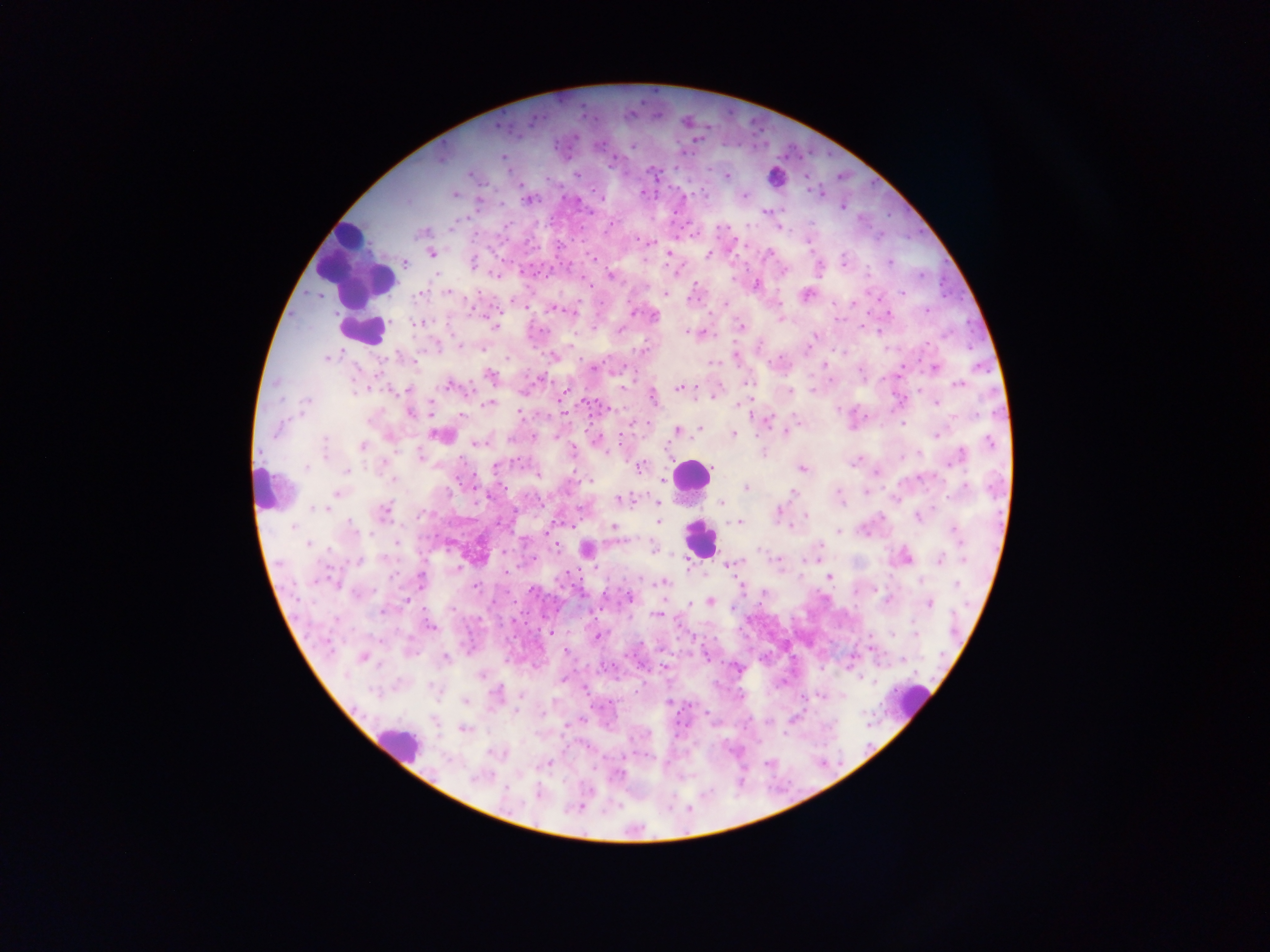 Approximate centers as [x, y] in pixels. Plasmodium parasite locations: [656, 91], [644, 100], [582, 105], [731, 110], [544, 114], [657, 115], [597, 118], [752, 120], [686, 122], [706, 124], [497, 125], [532, 126], [764, 131], [574, 137], [693, 141], [636, 144], [676, 144], [791, 144], [603, 150], [812, 152], [828, 153], [568, 155], [503, 156], [440, 158], [679, 165], [653, 173], [837, 175], [726, 176], [806, 178], [871, 181], [703, 186], [593, 190], [642, 192], [820, 192], [454, 194], [565, 194], [685, 195], [707, 195], [743, 196], [602, 197], [528, 199], [843, 206], [906, 209], [590, 211], [674, 212], [889, 213], [556, 215], [551, 224], [609, 226], [779, 226], [422, 232], [924, 233], [694, 234], [498, 235], [558, 237], [808, 238], [906, 238], [525, 240], [649, 243], [814, 250], [432, 253], [586, 253], [669, 253], [708, 254], [556, 256], [501, 258], [595, 259], [512, 260], [404, 262], [472, 262], [529, 262], [819, 262], [842, 262], [890, 262], [571, 263], [782, 270], [521, 273], [920, 273], [498, 274], [535, 274], [868, 274], [610, 275], [548, 278], [583, 278], [939, 281], [756, 284], [592, 285], [447, 291], [805, 293], [902, 293], [419, 294], [665, 294], [688, 299], [834, 301], [853, 301], [725, 305], [524, 306], [924, 308], [553, 309], [866, 310], [633, 312], [888, 314], [653, 315], [835, 317], [844, 317], [780, 319], [967, 319], [415, 322], [861, 325], [494, 326], [740, 327], [620, 330], [688, 331], [694, 332], [701, 332], [814, 336], [928, 340], [460, 346], [635, 346], [969, 346], [735, 355], [327, 357], [554, 357], [976, 362], [823, 365], [625, 366], [593, 368], [935, 368], [490, 376], [748, 383], [450, 384], [959, 384], [680, 388], [788, 391], [714, 394], [562, 397], [652, 397], [581, 399], [596, 399], [305, 402], [935, 402], [489, 404], [743, 404], [430, 408], [606, 408], [409, 410], [519, 410], [588, 416], [549, 419], [767, 419], [523, 421], [649, 422], [902, 424], [700, 429], [621, 430], [678, 431], [786, 432], [534, 434], [733, 434], [936, 434], [441, 435], [556, 435], [596, 439], [477, 442], [362, 447], [764, 454], [573, 455], [461, 458], [518, 459], [494, 465], [639, 467], [801, 468], [574, 470], [345, 472], [876, 472], [474, 475], [537, 477], [593, 477], [392, 480], [663, 481], [459, 484], [503, 487], [746, 488], [866, 492], [792, 493], [336, 494], [488, 495], [619, 499], [721, 503], [657, 504], [472, 505], [542, 505], [425, 510], [515, 511], [777, 511], [382, 512], [805, 516], [917, 516], [417, 519], [658, 521], [739, 521], [495, 524], [572, 524], [614, 527], [791, 527], [954, 528], [838, 532], [512, 534], [545, 535], [398, 541], [556, 544], [655, 548], [449, 550], [587, 550], [504, 553], [534, 557], [819, 558], [906, 558], [778, 559], [963, 559], [940, 560], [359, 561], [729, 563], [461, 566], [567, 568], [504, 570], [703, 573], [829, 577], [421, 579], [579, 580], [663, 582], [741, 583], [956, 584], [474, 585], [530, 586], [560, 586], [603, 592], [547, 594], [580, 596], [629, 596], [513, 598], [495, 599], [888, 599], [710, 602], [929, 602], [689, 604], [759, 605], [733, 606], [600, 609], [656, 614], [542, 615], [630, 618], [512, 621], [526, 622], [429, 626], [740, 628], [537, 630], [551, 632], [892, 633], [595, 634], [915, 634], [512, 638], [713, 638], [640, 642], [869, 647], [567, 651], [691, 652], [708, 656], [362, 657], [633, 657], [444, 658], [901, 659], [614, 664], [665, 668], [737, 668], [821, 668], [480, 675], [862, 678], [563, 679], [643, 681], [585, 689], [636, 690], [496, 694], [520, 695], [802, 698], [466, 701], [670, 703], [692, 703], [600, 708], [805, 710], [585, 712], [707, 714], [791, 720], [751, 721], [568, 723], [608, 724], [866, 725], [685, 726], [462, 728], [744, 728], [560, 734], [650, 734], [784, 734], [632, 737], [866, 743], [587, 749], [648, 755], [603, 757], [823, 761], [840, 761], [549, 763], [766, 764], [594, 768], [537, 794], [581, 804], [671, 807], [690, 807]. Leukocyte locations: [775, 177], [355, 267], [361, 324], [364, 330], [690, 476], [269, 488], [699, 537], [911, 700], [399, 744]. Image is 1270×952 pixels. Photographed through a microscope with a mobile-phone camera. Collected in Ghana. One field of view. Thick blood smear.